Assess this cell for malaria.
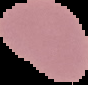

It is uninfected.

Image is 88×85 pixels. From a thin blood smear. The area outside the segmented cell region is set to black.